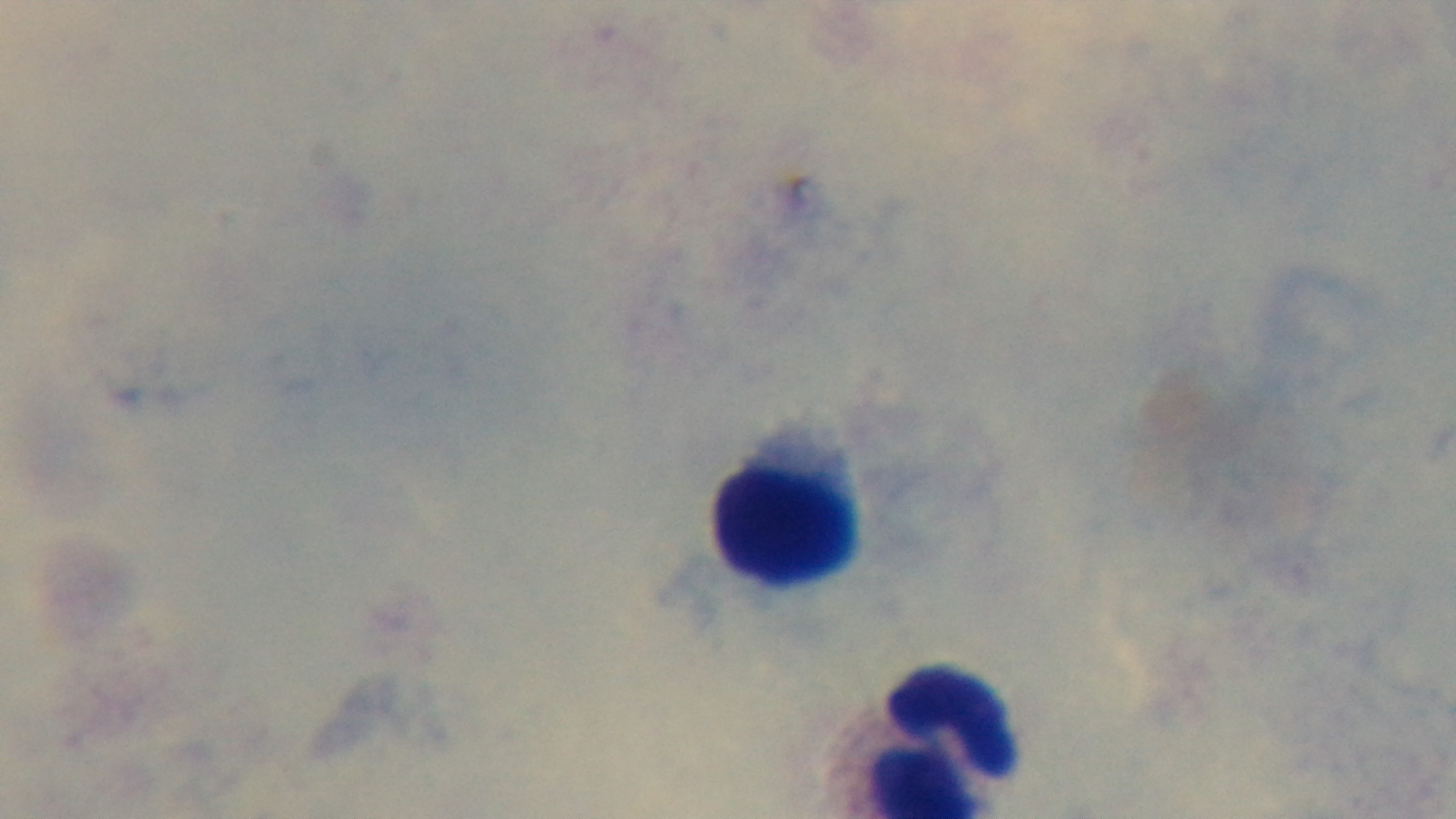
stain = Giemsa
preparation = thick blood film
capture = mounted 4K digital camera
objective = 100x oil immersion
modality = light microscopy
malaria status = negative
field of view = single